Classify this cell by malaria status.
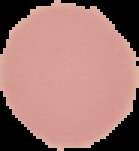
It is uninfected.

Summary:
  - Preparation: thin blood smear
  - Image size: 139×151 pixels
  - Image type: cell region segmented out of the field of view; surrounding area masked to black